Classify this cell by malaria status.
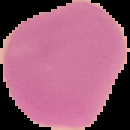

It is uninfected.

From a thin blood smear. The area outside the segmented cell region is set to black. Image is 130×130 pixels.